Report the malaria status of this cell.
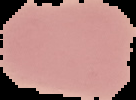

Uninfected.

preparation = thin blood smear
image size = 136×100 pixels
image type = segmented cell region with the area outside set to black